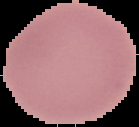
Summary:
  - Image size: 139×127 pixels
  - Result: no Plasmodium parasites seen
  - Preparation: thin blood smear
  - Image type: segmented cell region on a black background